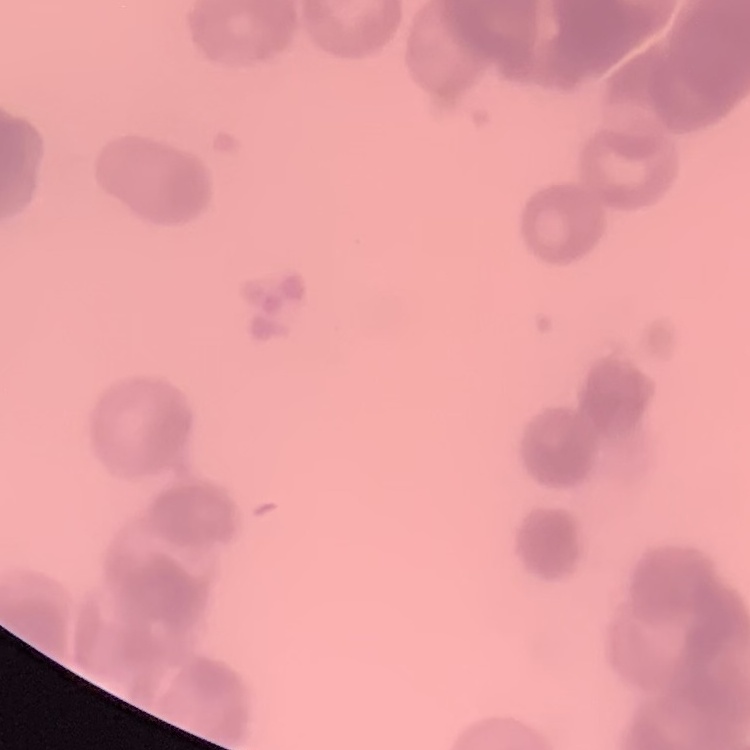
The erythrocytes show rouleaux formation. Square crop of a larger photomicrograph. Stained with either Field's or Giemsa. Thin blood smear.